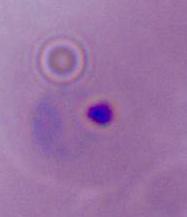
Summary:
  - Identification: Plasmodium
  - Magnification: 400x or 1000x
  - Modality: photomicrograph